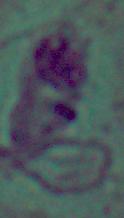

Summary:
  - Identification: Leishmania
  - Magnification: 1000x
  - Modality: photomicrograph